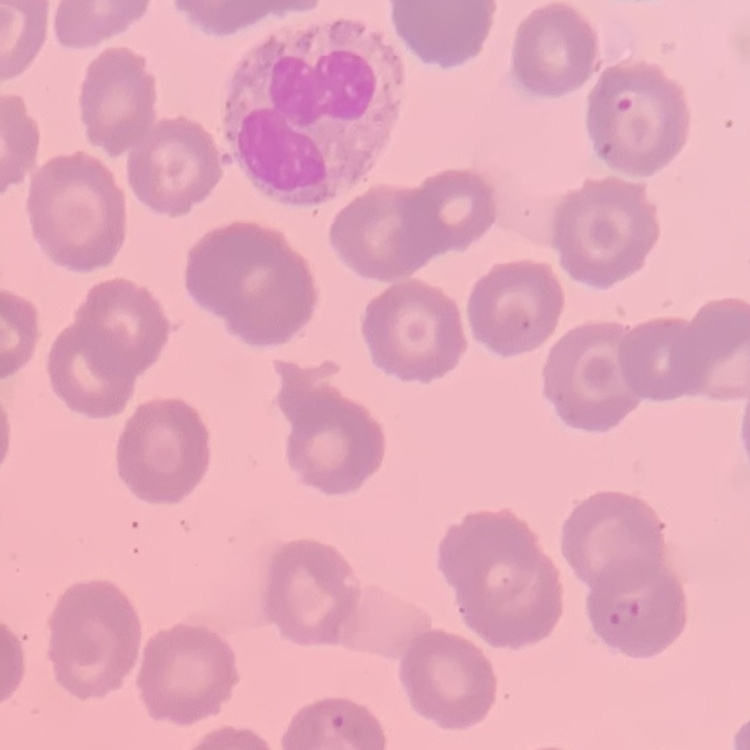

The erythrocytes exhibit no rouleaux formation. Field's or Giemsa stain. Thin blood smear. One tile cut from a larger photomicrograph.